Assess this cell for malaria.
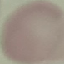
Uninfected.

Summary:
  - Image type: cell patch, automatically extracted from a larger field of view and resized to 64 × 64 pixels
  - Capture: smartphone camera at the microscope eyepiece
  - Stain: Giemsa
  - Preparation: thin blood film